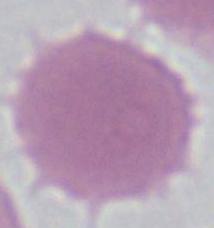

Summary:
  - Identification: erythrocyte
  - Magnification: 1000x
  - Modality: photomicrograph